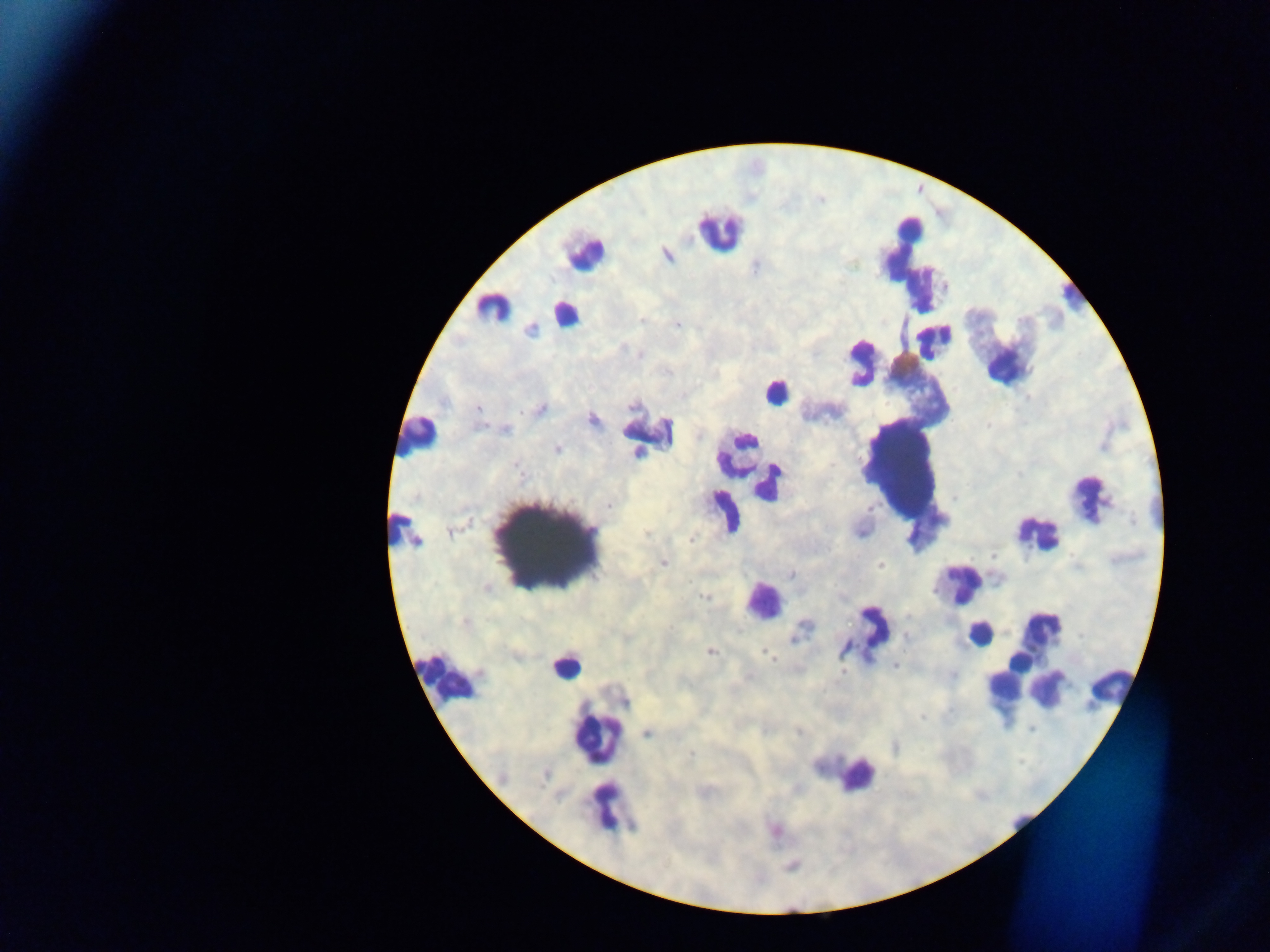

capture = mobile-phone photograph through a microscope
image size = 1270×952 pixels
preparation = thick blood film
leukocyte locations = approximate centers as (x, y) in pixels: (718, 231), (583, 252), (911, 256), (1068, 294), (491, 306), (564, 314), (996, 340), (935, 342), (861, 362), (775, 391), (647, 430), (418, 436), (735, 454), (902, 471), (771, 482), (1088, 498), (728, 509), (397, 524), (1036, 532), (551, 543), (962, 583), (762, 601), (872, 632), (978, 634), (564, 665), (1042, 668), (447, 676), (1049, 687), (1111, 690), (1009, 697), (598, 738), (856, 775), (610, 809)
country = Ghana
Plasmodium parasite locations = approximate centers as (x, y) in pixels: (667, 255), (642, 319), (677, 324), (531, 330), (641, 355), (633, 406), (478, 409), (539, 409), (592, 420), (506, 429), (699, 435), (557, 450), (638, 452), (519, 471), (610, 506), (451, 531), (860, 532), (646, 534), (691, 539), (416, 542), (993, 555), (664, 563), (880, 565), (791, 574), (487, 587), (704, 596), (464, 622), (805, 626), (905, 637), (794, 638), (846, 648), (711, 651), (767, 654), (894, 665), (842, 671), (952, 675), (624, 700), (922, 717), (799, 732), (648, 733), (691, 755), (704, 792)
field of view = single